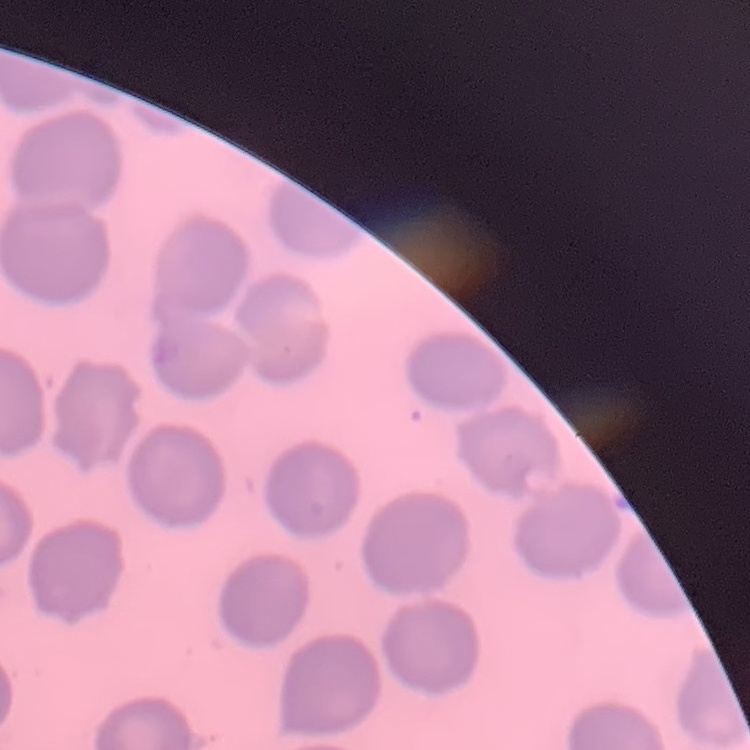

The red blood cells exhibit no rouleaux formation. Thin blood smear. Stained with either Field's or Giemsa. One tile cut from a larger photomicrograph.